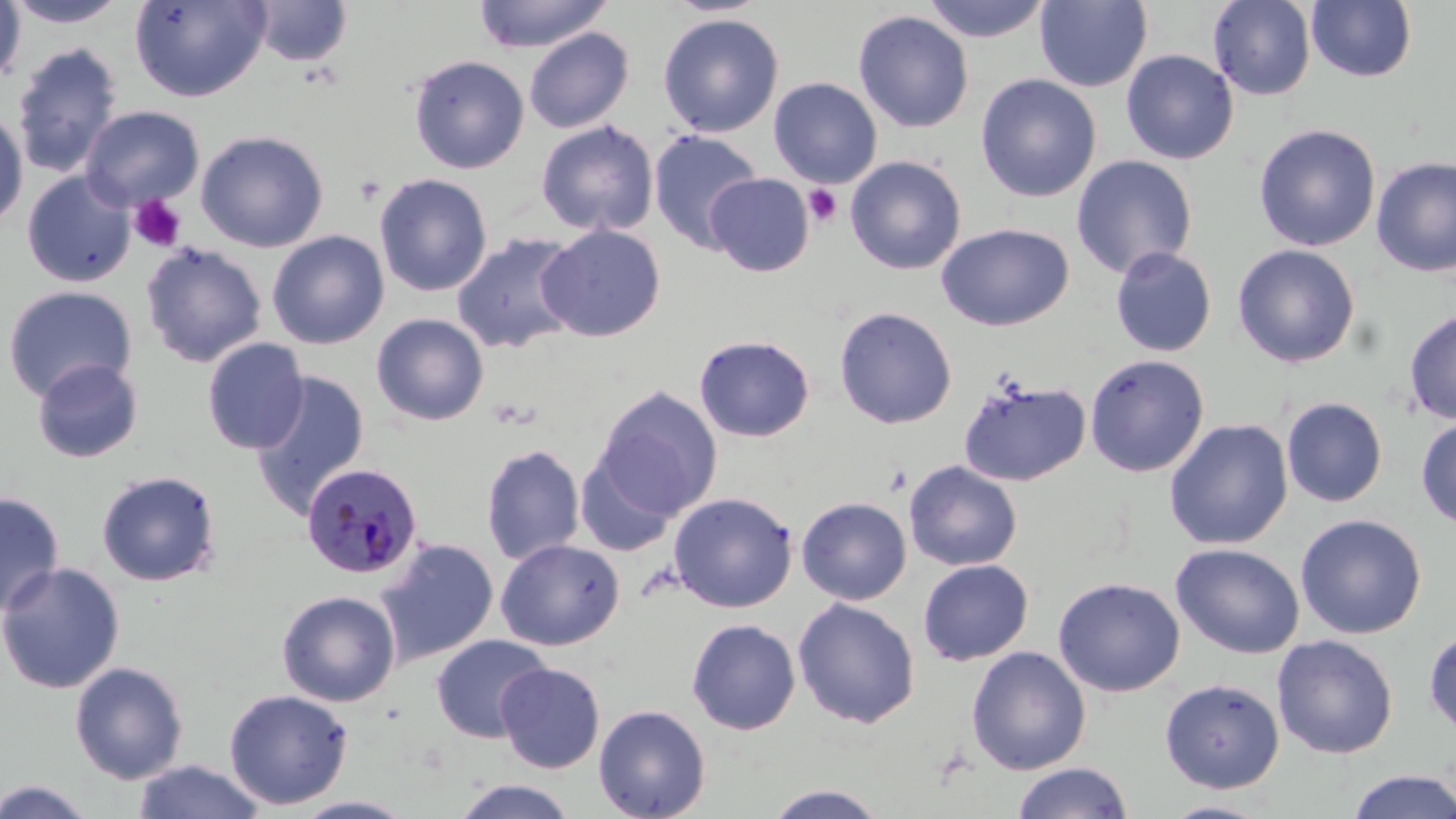
Summary:
  - Coordinate format: approximate bounding boxes as [x1, y1, x2, y2] in pixels
  - Platelet locations: [803, 184, 843, 227], [128, 195, 186, 253]
  - Plasmodium malariae-infected red blood cell locations: [301, 462, 423, 580]
  - Uninfected red blood cell locations: [130, 0, 270, 102], [473, 0, 613, 53], [921, 0, 1053, 42], [1208, 0, 1316, 101], [1306, 0, 1417, 82], [0, 1, 26, 87], [4, 1, 131, 28], [249, 1, 353, 67], [1034, 1, 1152, 92], [852, 10, 974, 133], [657, 12, 784, 137], [523, 27, 634, 133], [11, 42, 122, 178], [1121, 49, 1239, 164], [409, 54, 530, 174], [975, 73, 1102, 202], [768, 76, 883, 188], [81, 105, 204, 211], [0, 109, 28, 233], [535, 119, 659, 237], [1253, 123, 1381, 252], [195, 130, 329, 253], [647, 130, 763, 253], [1071, 154, 1198, 279], [845, 155, 967, 275], [1371, 156, 1456, 278], [21, 171, 135, 287], [374, 173, 492, 297], [705, 173, 814, 276], [936, 223, 1074, 332], [536, 224, 666, 342], [267, 230, 390, 349], [451, 231, 583, 354], [140, 243, 267, 368], [1232, 244, 1360, 368], [1110, 245, 1218, 358], [1, 285, 138, 403], [834, 306, 958, 429], [1403, 308, 1456, 425], [371, 313, 489, 426], [694, 335, 815, 442], [202, 338, 309, 454], [1084, 353, 1210, 477], [32, 358, 143, 464], [249, 370, 370, 518], [958, 378, 1091, 487], [593, 386, 722, 520], [1280, 396, 1388, 507], [1416, 415, 1456, 530], [1164, 418, 1294, 550], [481, 443, 586, 565], [575, 452, 680, 557], [903, 460, 1023, 571], [96, 469, 221, 587], [0, 491, 64, 617], [667, 491, 798, 613], [796, 496, 912, 605], [1294, 513, 1427, 639], [375, 538, 499, 667], [495, 538, 625, 651], [1170, 542, 1305, 659], [917, 558, 1034, 665], [0, 562, 125, 694], [1052, 576, 1185, 697], [276, 590, 401, 707], [792, 597, 920, 729], [686, 618, 801, 735], [1423, 626, 1456, 741], [430, 633, 553, 743], [1272, 634, 1398, 758], [966, 645, 1091, 775], [69, 661, 189, 784], [495, 662, 606, 773], [1159, 677, 1285, 793], [223, 688, 353, 809], [593, 704, 711, 818], [132, 759, 267, 819], [1011, 762, 1133, 819], [1345, 770, 1456, 819], [1, 778, 98, 819], [450, 778, 578, 818], [762, 784, 892, 818], [291, 795, 419, 818], [1159, 800, 1276, 818]
  - Slide-level diagnosis: Plasmodium malariae
  - Magnification: 1000x
  - Modality: optical microscopy
  - Stain: May-Grünwald-Giemsa
  - Image size: 1456×819 pixels
  - Field of view: one of a larger specimen
  - Preparation: thin blood smear